Locate and identify every blood parasite.
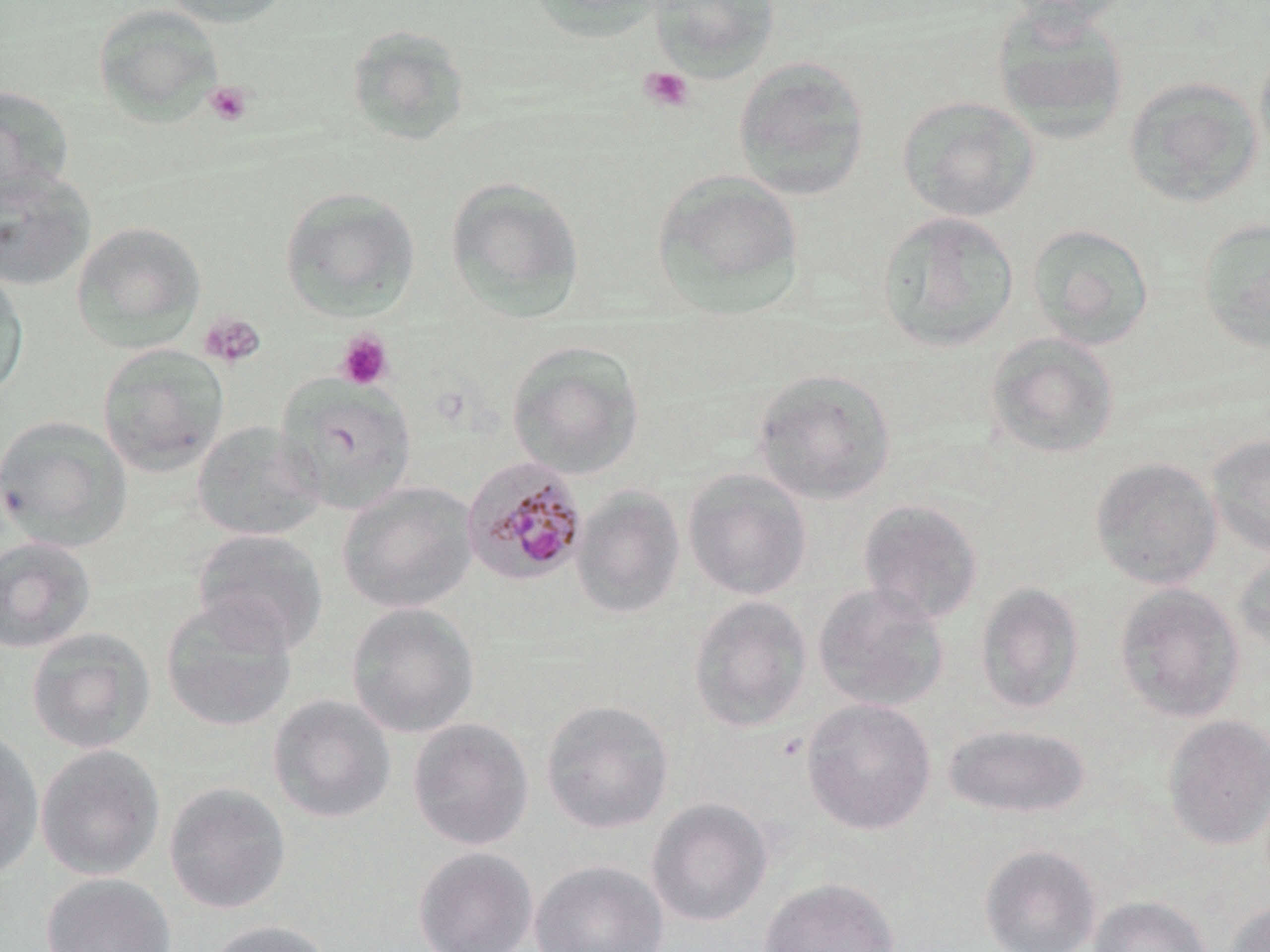

Approximate bounding boxes as (x1,y1)-(x2,y2) corner pairs in pixels.
Plasmodium malariae-infected red blood cells: (462,457)-(588,587).
No Plasmodium falciparum, Plasmodium ovale, Plasmodium vivax, Babesia divergens, or Trypanosoma brucei observed.

Summary:
  - Uninfected red blood cell locations: (164,0)-(293,28), (529,0)-(667,43), (649,0)-(780,81), (998,0)-(1136,27), (92,4)-(223,127), (991,4)-(1129,144), (344,24)-(472,147), (1254,41)-(1270,166), (733,56)-(872,200), (1123,76)-(1263,208), (0,85)-(75,202), (897,95)-(1040,222), (0,167)-(96,291), (651,169)-(804,316), (445,176)-(586,322), (279,186)-(421,322), (877,211)-(1019,353), (1196,217)-(1270,353), (71,221)-(206,352), (1026,223)-(1155,350), (0,267)-(30,401), (985,332)-(1120,460), (506,340)-(645,481), (97,343)-(230,477), (751,368)-(897,505), (275,374)-(418,514), (0,415)-(133,551), (192,420)-(325,541), (1206,433)-(1270,557), (1090,456)-(1223,589), (683,468)-(812,601), (337,481)-(479,614), (572,487)-(685,619), (858,499)-(984,625), (191,528)-(328,655), (0,536)-(97,654), (1233,547)-(1270,654), (975,582)-(1085,715), (812,583)-(950,713), (1113,583)-(1245,723), (688,595)-(812,733), (160,597)-(298,731), (346,602)-(479,738), (26,628)-(156,754), (268,693)-(396,824), (801,698)-(936,835), (540,699)-(674,834), (1162,715)-(1270,851), (407,717)-(534,851), (943,723)-(1092,819), (0,728)-(44,879), (35,744)-(165,881), (163,782)-(291,915), (646,797)-(773,928), (979,844)-(1102,952), (413,847)-(538,952), (530,859)-(669,952), (41,872)-(176,952), (760,877)-(900,952), (1088,895)-(1214,952), (1225,900)-(1270,952), (205,920)-(334,952)
  - Platelet locations: (639,66)-(695,113), (204,80)-(254,126), (199,312)-(266,369), (335,330)-(394,391)
  - Slide-level diagnosis: Plasmodium malariae
  - Magnification: 1000x
  - Preparation: thin blood smear
  - Modality: optical microscopy
  - Stain: May-Grünwald-Giemsa
  - Image size: 1270×952 pixels
  - Field of view: one of a larger specimen